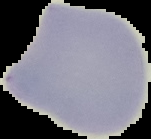

Summary:
  - Malaria status: uninfected
  - Preparation: thin blood film
  - Image type: cell region segmented out of the field of view; surrounding area masked to black
  - Image size: 151×139 pixels